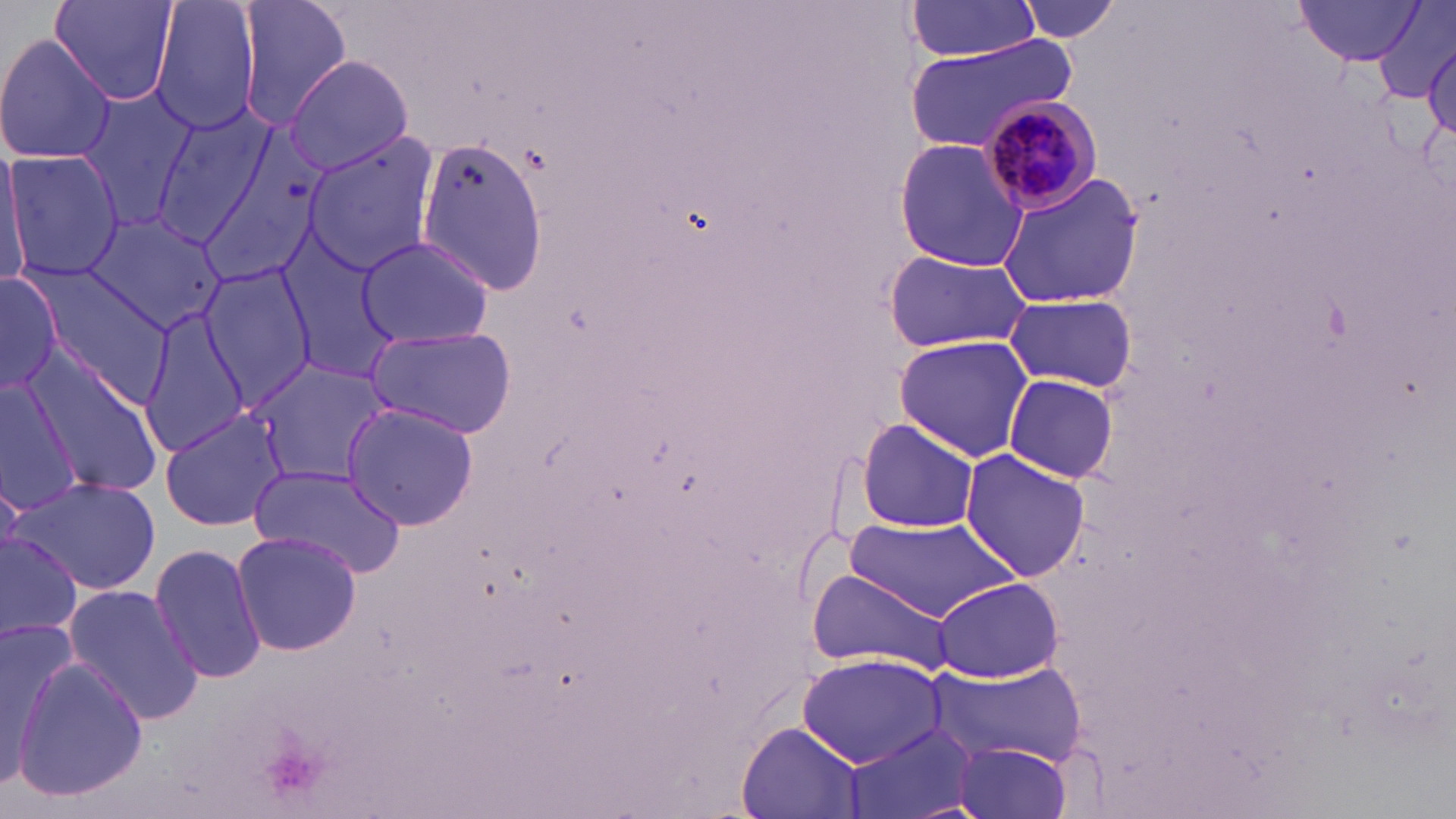
Summary:
  - Coordinate format: approximate bounding boxes as (x1, y1, x2, y2) in pixels
  - Uninfected red blood cell locations: (50, 0, 180, 107), (150, 0, 261, 134), (235, 0, 354, 130), (1016, 0, 1122, 45), (1294, 1, 1426, 65), (906, 2, 1042, 61), (1375, 3, 1456, 105), (0, 33, 119, 167), (905, 35, 1076, 154), (1424, 40, 1456, 140), (284, 53, 414, 175), (77, 85, 200, 231), (151, 110, 274, 249), (192, 133, 331, 294), (299, 133, 440, 278), (415, 134, 551, 298), (892, 136, 1029, 272), (1, 143, 30, 288), (6, 149, 120, 280), (992, 169, 1145, 309), (84, 211, 228, 332), (355, 235, 495, 348), (277, 236, 402, 382), (882, 251, 1033, 351), (25, 260, 171, 398), (198, 261, 318, 404), (0, 266, 70, 397), (1001, 293, 1139, 394), (138, 306, 252, 457), (364, 324, 518, 441), (892, 335, 1034, 461), (24, 350, 161, 497), (251, 360, 389, 486), (1003, 373, 1119, 484), (0, 377, 82, 515), (338, 404, 483, 531), (160, 408, 292, 532), (854, 418, 984, 533), (958, 449, 1092, 580), (247, 466, 405, 574), (14, 475, 160, 594), (846, 517, 1021, 621), (229, 529, 364, 657), (0, 531, 82, 644), (149, 541, 266, 685), (806, 569, 955, 673), (931, 577, 1065, 682), (62, 583, 204, 725), (0, 625, 79, 793), (797, 653, 948, 769), (10, 655, 150, 801), (926, 660, 1083, 763), (736, 722, 862, 818), (839, 723, 983, 819), (947, 740, 1076, 819)
  - Plasmodium malariae-infected red blood cell locations: (980, 98, 1106, 214)
  - Slide-level diagnosis: Plasmodium malariae
  - Field of view: single
  - Magnification: 1000x
  - Stain: May-Grünwald-Giemsa
  - Modality: optical microscopy
  - Image size: 1456×819 pixels
  - Preparation: thin blood smear